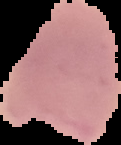
{
  "result": "malaria parasites identified",
  "preparation": "thin blood film",
  "image_size": "121×145 pixels",
  "image_type": "cell region segmented out of the field of view; surrounding area masked to black"
}